Name the blood parasite species.
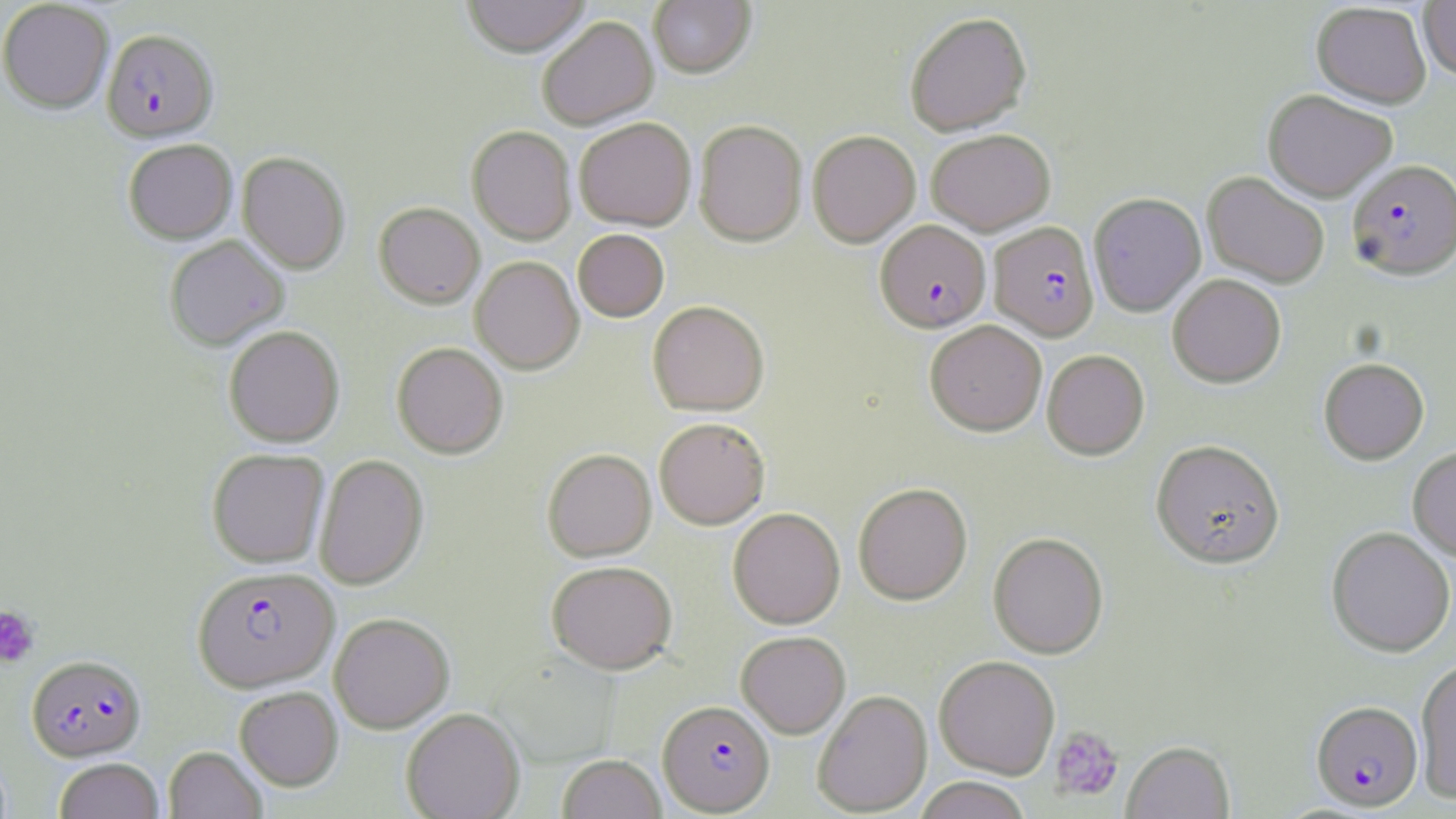

Plasmodium falciparum.

field of view = one of a larger specimen
modality = optical microscopy
platelet locations = approximate bounding boxes as (x1, y1, x2, y2) in pixels: (0, 606, 39, 668), (1049, 725, 1124, 802)
stain = May-Grünwald-Giemsa
preparation = thin blood smear
Plasmodium falciparum-infected red blood cell locations = approximate bounding boxes as (x1, y1, x2, y2) in pixels: (102, 29, 218, 142), (1347, 159, 1456, 280), (875, 220, 991, 332), (989, 221, 1099, 341), (192, 566, 338, 692), (27, 654, 146, 762), (658, 700, 775, 814), (1311, 700, 1423, 811)
magnification = 1000x
image size = 1456×819 pixels
uninfected red blood cell locations = approximate bounding boxes as (x1, y1, x2, y2) in pixels: (0, 0, 114, 113), (460, 0, 592, 57), (649, 0, 756, 78), (1418, 0, 1456, 80), (1311, 2, 1431, 108), (904, 12, 1032, 135), (537, 16, 658, 129), (1263, 89, 1397, 201), (574, 117, 696, 230), (694, 120, 807, 246), (467, 126, 576, 244), (926, 129, 1055, 234), (807, 130, 920, 247), (123, 138, 237, 244), (237, 151, 350, 274), (1202, 171, 1329, 288), (1088, 186, 1328, 301), (1088, 192, 1206, 316), (374, 202, 484, 308), (572, 229, 669, 322), (164, 236, 289, 350), (470, 256, 584, 374), (1167, 274, 1286, 387), (647, 300, 769, 416), (925, 319, 1047, 435), (224, 325, 345, 447), (391, 342, 508, 458), (1041, 349, 1149, 459), (1319, 358, 1429, 464), (654, 417, 770, 529), (1151, 439, 1285, 568), (1408, 445, 1456, 561), (207, 448, 329, 568), (542, 449, 657, 561), (314, 454, 429, 590), (853, 482, 973, 605), (727, 507, 845, 628), (1326, 527, 1455, 657), (988, 532, 1108, 659), (546, 560, 678, 674), (329, 612, 454, 733), (736, 631, 850, 738), (934, 655, 1060, 779), (1415, 658, 1456, 803), (235, 686, 343, 791), (812, 690, 932, 816), (401, 707, 524, 819), (1122, 740, 1235, 819), (164, 746, 267, 819), (557, 754, 667, 819), (53, 757, 164, 819), (912, 777, 1033, 819)